State the blood parasite species.
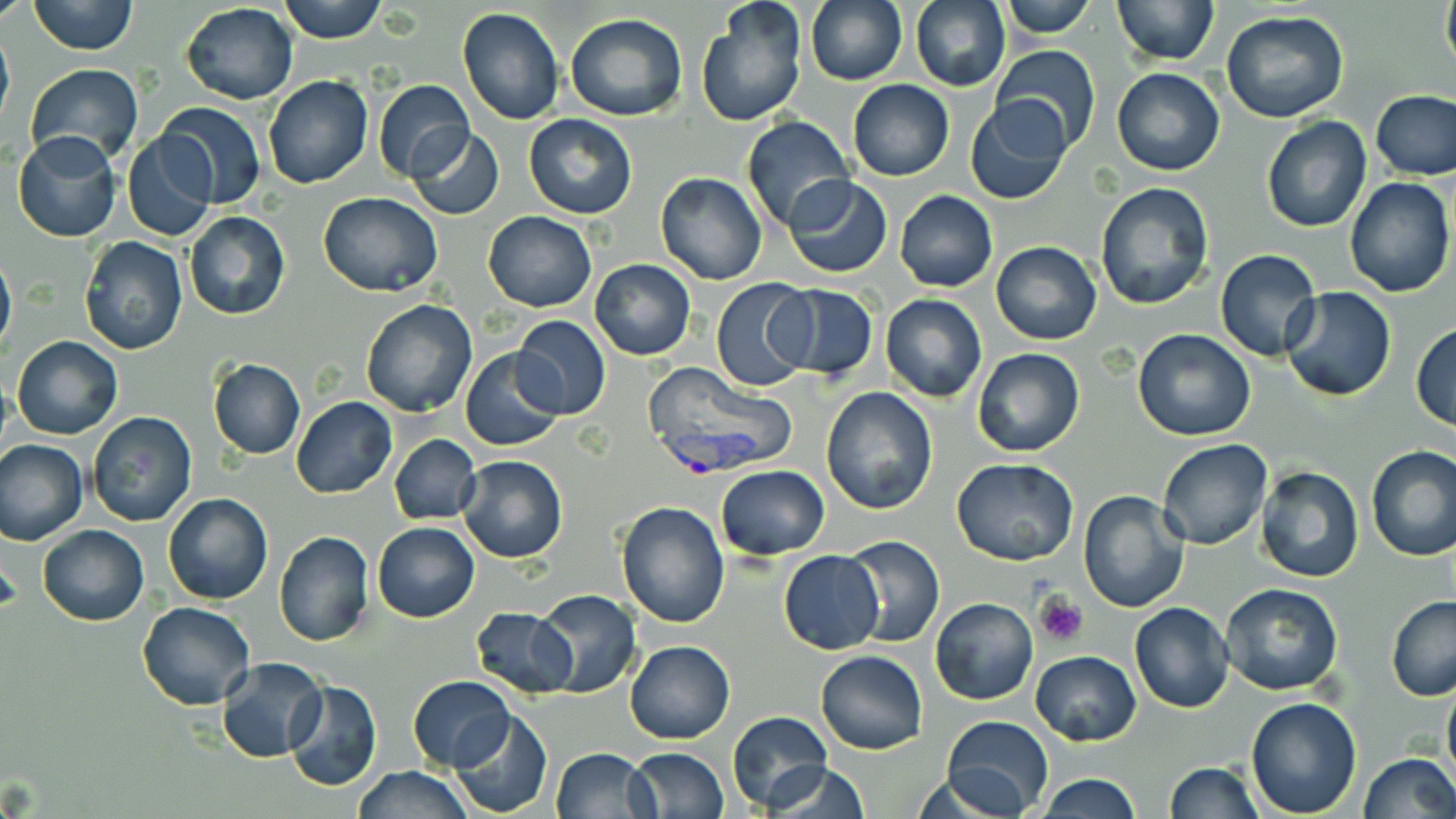
Plasmodium vivax.

Approximate bounding boxes as [x1, y1, x2, y2] in pixels. Uninfected red blood cell locations: [0, 0, 30, 25], [28, 0, 140, 55], [278, 0, 386, 44], [910, 0, 1010, 92], [999, 0, 1097, 38], [1112, 0, 1219, 64], [1440, 0, 1456, 79], [805, 1, 907, 85], [180, 3, 299, 104], [697, 4, 807, 127], [457, 6, 565, 125], [1221, 11, 1350, 124], [565, 14, 689, 121], [0, 24, 14, 136], [991, 46, 1103, 155], [25, 64, 143, 167], [1112, 66, 1224, 176], [263, 75, 374, 188], [372, 79, 475, 181], [848, 79, 953, 181], [1371, 88, 1456, 180], [967, 97, 1071, 204], [155, 102, 268, 208], [523, 114, 636, 219], [741, 116, 853, 230], [1261, 118, 1370, 233], [407, 127, 505, 220], [12, 132, 122, 243], [123, 133, 217, 242], [655, 172, 767, 284], [783, 175, 891, 276], [1344, 176, 1454, 299], [1095, 182, 1217, 313], [894, 190, 997, 293], [319, 191, 442, 296], [184, 211, 290, 320], [482, 211, 596, 311], [79, 235, 188, 355], [991, 240, 1101, 345], [0, 250, 16, 356], [1215, 250, 1323, 362], [589, 259, 695, 360], [712, 277, 816, 393], [775, 284, 878, 382], [1282, 287, 1397, 402], [880, 294, 986, 402], [360, 298, 477, 418], [511, 316, 612, 420], [1411, 323, 1455, 432], [1132, 329, 1257, 441], [12, 335, 122, 440], [972, 347, 1085, 457], [460, 348, 567, 452], [208, 359, 306, 459], [820, 388, 937, 514], [292, 396, 397, 498], [85, 411, 197, 528], [388, 433, 481, 526], [0, 437, 88, 545], [1156, 437, 1273, 551], [1367, 447, 1456, 561], [458, 455, 567, 563], [951, 459, 1077, 567], [1254, 464, 1363, 583], [715, 465, 828, 559], [1077, 490, 1191, 613], [163, 494, 273, 605], [615, 499, 731, 627], [371, 521, 479, 622], [38, 524, 148, 625], [275, 530, 375, 647], [840, 533, 945, 648], [778, 550, 883, 655], [1219, 581, 1345, 696], [533, 589, 640, 697], [1385, 596, 1456, 701], [931, 597, 1039, 705], [138, 601, 254, 710], [1129, 603, 1235, 713], [470, 606, 577, 698], [626, 640, 735, 744], [815, 650, 927, 755], [1030, 650, 1142, 745], [217, 656, 329, 763], [408, 675, 515, 771], [1442, 677, 1456, 793], [283, 680, 382, 792], [1245, 696, 1362, 816], [728, 710, 833, 811], [449, 711, 553, 818], [940, 714, 1052, 817], [551, 747, 657, 819], [625, 747, 729, 819], [1357, 753, 1456, 819], [1163, 761, 1263, 818], [761, 762, 871, 819], [350, 765, 473, 819], [1036, 774, 1141, 818]. Plasmodium vivax-infected red blood cell locations: [640, 364, 797, 473]. Platelet locations: [1033, 592, 1089, 647]. Image is 1456×819 pixels. One field of a larger specimen. 1000x magnification. Optical microscopy. Thin blood smear. May-Grünwald-Giemsa stain.